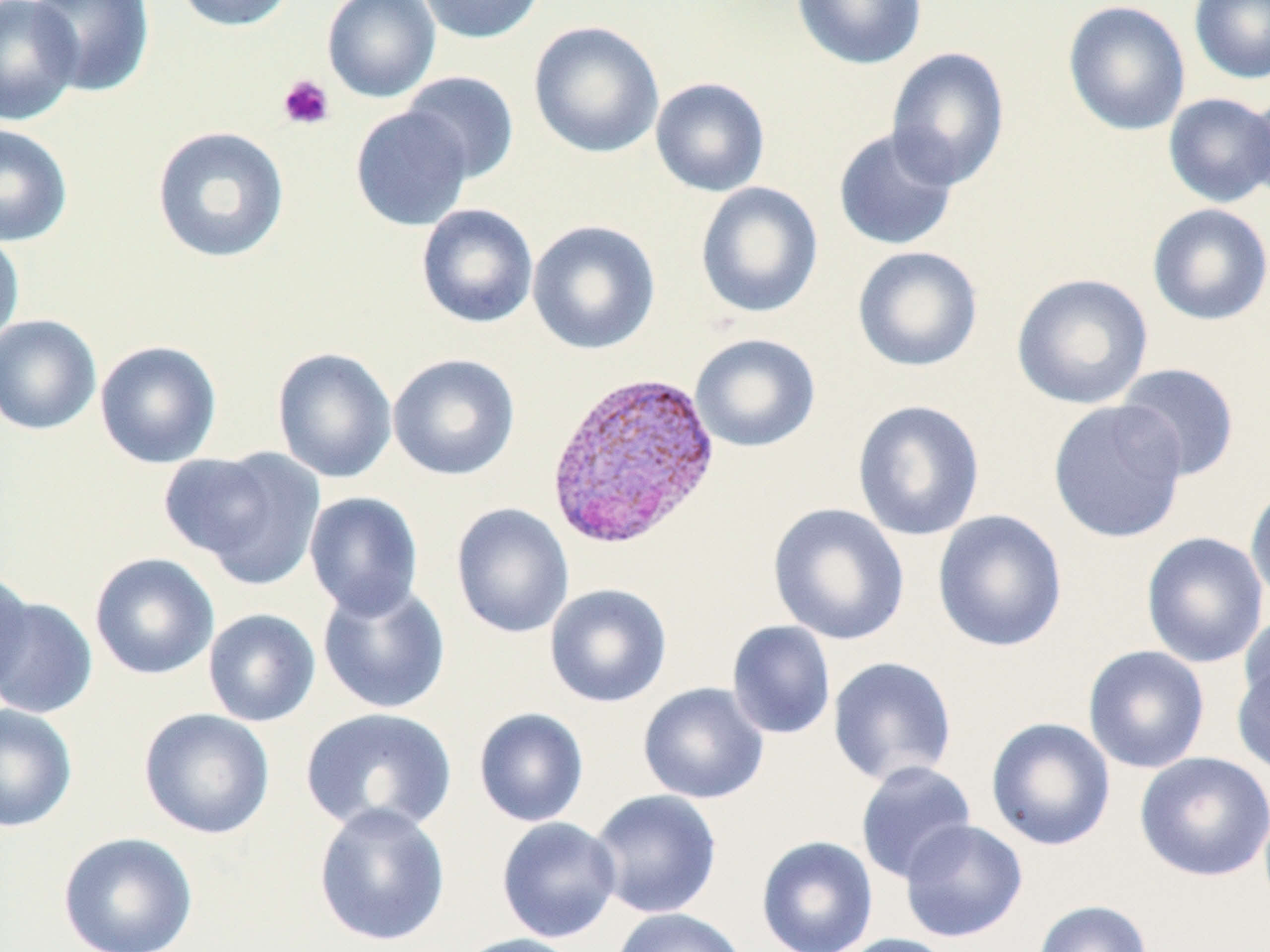

Approximate bounding boxes as (x1,y1)-(x2,y2) corner pairs in pixels. Platelet locations: (277,73)-(335,131). Plasmodium vivax-infected red blood cell locations: (545,368)-(722,550). Uninfected red blood cell locations: (0,0)-(82,126), (27,0)-(156,97), (171,0)-(297,32), (321,0)-(441,103), (416,0)-(547,44), (791,0)-(928,70), (1188,0)-(1270,84), (1062,1)-(1191,136), (528,20)-(664,159), (886,46)-(1011,190), (401,70)-(520,184), (650,77)-(770,197), (1244,88)-(1270,210), (1163,93)-(1270,208), (349,106)-(473,232), (0,123)-(73,247), (151,125)-(291,264), (832,127)-(960,252), (694,181)-(824,319), (415,203)-(539,329), (1147,203)-(1270,327), (527,219)-(661,355), (0,229)-(25,350), (851,245)-(984,373), (1011,272)-(1154,410), (0,315)-(101,436), (689,333)-(821,453), (94,340)-(222,469), (271,347)-(398,483), (387,353)-(520,481), (1115,362)-(1240,482), (851,399)-(985,541), (1047,400)-(1188,543), (168,446)-(326,588), (1245,480)-(1270,611), (304,491)-(424,618), (451,503)-(574,639), (767,503)-(910,646), (932,509)-(1068,653), (1140,531)-(1269,668), (89,553)-(219,681), (0,569)-(35,694), (316,578)-(451,714), (544,583)-(672,708), (0,595)-(98,719), (202,608)-(321,727), (1239,611)-(1270,720), (726,620)-(836,740), (1082,645)-(1211,774), (827,656)-(958,786), (1232,657)-(1269,778), (638,682)-(770,805), (0,703)-(78,833), (138,707)-(275,840), (299,707)-(458,836), (473,708)-(589,827), (985,717)-(1116,851), (1134,751)-(1270,882), (855,760)-(977,884), (589,789)-(722,919), (313,802)-(451,947), (496,816)-(622,943), (899,819)-(1028,943), (58,832)-(198,952), (756,835)-(879,952), (1033,900)-(1153,952), (610,907)-(750,952), (452,933)-(587,952), (832,933)-(961,952). Slide-level diagnosis: Plasmodium vivax. Light microscopy. One field of a larger specimen. Thin blood film. Image is 1270×952 pixels. May-Grünwald-Giemsa-stained preparation. Captured at 1000x magnification.